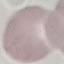
malaria_status: uninfected
image_type: cell patch, automatically extracted from a larger field of view and resized to 64 × 64 pixels
preparation: thin blood film
capture: smartphone camera at the microscope eyepiece
stain: Giemsa